Give the position of every Plasmodium parasite and every leukocyte.
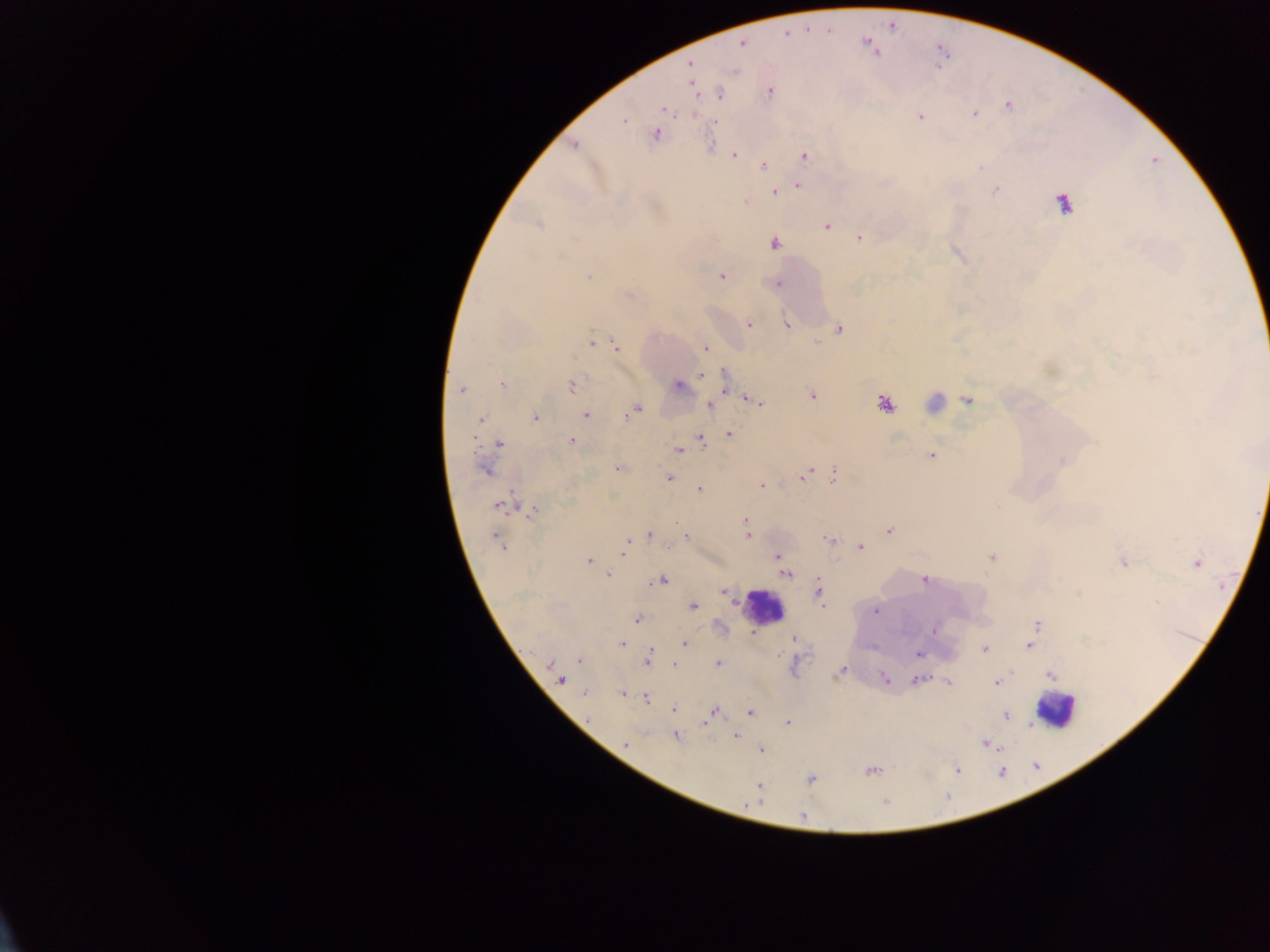

Approximate centers as x y in pixels.
Plasmodium parasites: 785 34; 742 43; 690 65; 693 84; 769 92; 720 94; 1008 105; 664 109; 974 113; 920 117; 624 120; 715 121; 655 134; 574 145; 734 156; 805 156; 763 166; 979 168; 798 185; 996 190; 774 192; 745 203; 1064 203; 539 225; 827 227; 859 237; 773 243; 588 277; 721 277; 778 284; 628 294; 748 325; 786 325; 839 329; 591 341; 818 342; 617 347; 705 348; 703 373; 725 377; 501 383; 571 385; 678 386; 461 390; 812 397; 967 400; 754 401; 884 404; 709 405; 635 408; 628 413; 586 415; 535 417; 480 420; 729 434; 473 437; 702 439; 572 441; 498 444; 679 450; 931 455; 619 468; 484 470; 804 474; 834 475; 669 478; 762 485; 699 489; 499 505; 533 512; 745 520; 889 531; 649 535; 747 536; 686 537; 498 540; 828 540; 627 542; 860 547; 624 553; 778 556; 992 557; 589 561; 1123 562; 1197 564; 785 574; 608 575; 662 580; 924 580; 724 591; 819 592; 693 606; 875 611; 637 619; 1037 624; 934 629; 753 633; 794 639; 621 643; 685 644; 1029 646; 985 650; 650 652; 918 654; 579 661; 647 662; 718 663; 549 665; 674 665; 842 670; 1051 674; 885 679; 560 680; 919 680; 949 682; 997 683; 584 693; 622 695; 646 699; 674 710; 714 711; 750 713; 1006 715; 709 718; 788 722; 735 735; 675 736; 626 744; 985 744; 761 750; 957 770; 871 771; 811 780; 760 785; 802 816.
Leukocytes: 933 402; 763 606; 1054 709.

Thick blood smear. Image is 1270×952 pixels. Photographed through a microscope with a mobile-phone camera. Collected in Ghana. Single field of view.